Name the parasite shown.
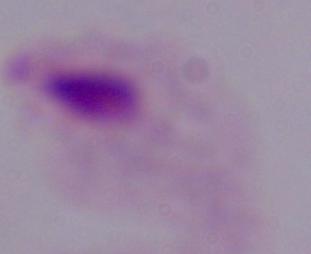
A trichomonad.

Captured at 1000x magnification. Photomicrograph.